Assess this cell for malaria.
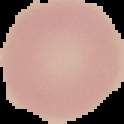
It is uninfected.

{
  "image_size": "124×124 pixels",
  "image_type": "segmented cell region on a black background",
  "preparation": "thin blood film"
}